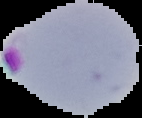

Segmented cell region on a black background. Image is 142×118 pixels. From a thin blood smear. Result: Plasmodium parasites detected.